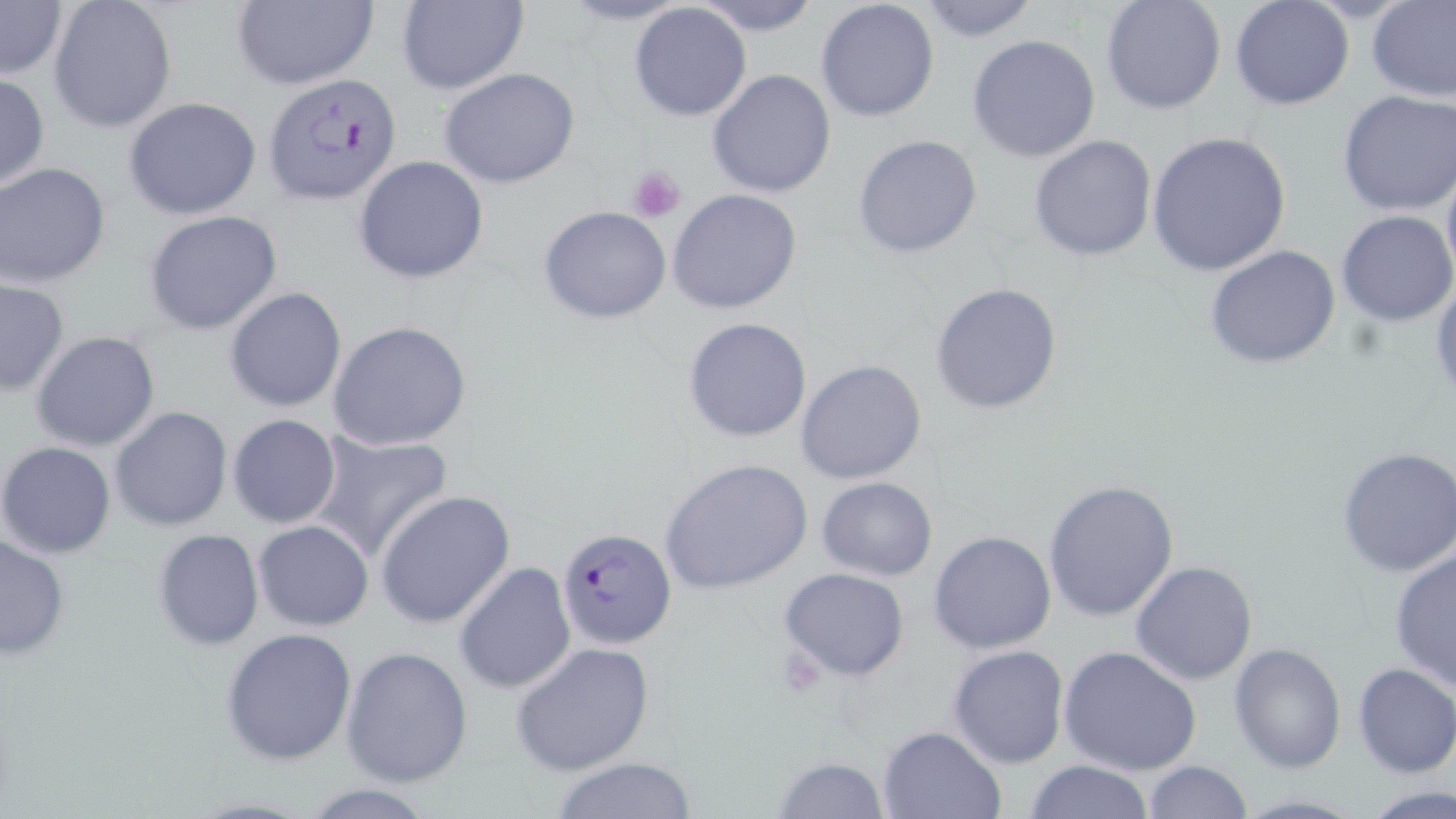

slide_level_diagnosis: Plasmodium falciparum
field_of_view: single
magnification: 1000x
preparation: thin blood smear
stain: May-Grünwald-Giemsa
platelet_locations: 'approximate bounding boxes as named x1/y1/x2/y2 corners in pixels: (x1=627, y1=165, x2=686, y2=221), (x1=774, y1=647, x2=825, y2=693)'
modality: light microscopy
plasmodium_falciparum_infected_red_blood_cell_locations: 'approximate bounding boxes as named x1/y1/x2/y2 corners in pixels: (x1=263, y1=73, x2=405, y2=205), (x1=555, y1=526, x2=676, y2=649)'
uninfected_red_blood_cell_locations: 'approximate bounding boxes as named x1/y1/x2/y2 corners in pixels: (x1=48, y1=0, x2=177, y2=134), (x1=691, y1=0, x2=824, y2=34), (x1=815, y1=0, x2=941, y2=122), (x1=913, y1=0, x2=1041, y2=42), (x1=1099, y1=0, x2=1226, y2=116), (x1=1230, y1=0, x2=1355, y2=111), (x1=229, y1=1, x2=379, y2=90), (x1=393, y1=1, x2=530, y2=94), (x1=1367, y1=1, x2=1456, y2=103), (x1=0, y1=2, x2=67, y2=81), (x1=628, y1=3, x2=752, y2=122), (x1=967, y1=35, x2=1100, y2=162), (x1=439, y1=67, x2=580, y2=188), (x1=707, y1=69, x2=837, y2=196), (x1=0, y1=73, x2=49, y2=191), (x1=1336, y1=91, x2=1456, y2=215), (x1=122, y1=96, x2=261, y2=220), (x1=1146, y1=131, x2=1291, y2=275), (x1=853, y1=133, x2=983, y2=259), (x1=1029, y1=134, x2=1157, y2=261), (x1=354, y1=155, x2=490, y2=284), (x1=1441, y1=163, x2=1456, y2=290), (x1=1, y1=164, x2=111, y2=287), (x1=668, y1=189, x2=803, y2=314), (x1=538, y1=205, x2=672, y2=324), (x1=144, y1=209, x2=284, y2=336), (x1=1336, y1=210, x2=1456, y2=326), (x1=1204, y1=245, x2=1344, y2=371), (x1=0, y1=279, x2=69, y2=395), (x1=931, y1=281, x2=1063, y2=415), (x1=225, y1=287, x2=347, y2=412), (x1=683, y1=316, x2=813, y2=443), (x1=328, y1=319, x2=475, y2=452), (x1=32, y1=331, x2=161, y2=451), (x1=796, y1=359, x2=928, y2=486), (x1=111, y1=407, x2=233, y2=531), (x1=228, y1=414, x2=341, y2=528), (x1=309, y1=430, x2=453, y2=564), (x1=0, y1=441, x2=117, y2=559), (x1=1336, y1=446, x2=1456, y2=578), (x1=660, y1=457, x2=813, y2=596), (x1=816, y1=477, x2=938, y2=581), (x1=1044, y1=479, x2=1180, y2=621), (x1=375, y1=491, x2=516, y2=629), (x1=254, y1=521, x2=373, y2=631), (x1=151, y1=527, x2=264, y2=651), (x1=928, y1=531, x2=1057, y2=654), (x1=0, y1=535, x2=70, y2=662), (x1=1389, y1=547, x2=1456, y2=693), (x1=1130, y1=560, x2=1257, y2=685), (x1=454, y1=563, x2=577, y2=694), (x1=779, y1=567, x2=910, y2=681), (x1=220, y1=627, x2=358, y2=765), (x1=1228, y1=641, x2=1345, y2=773), (x1=510, y1=642, x2=656, y2=776), (x1=947, y1=644, x2=1070, y2=767), (x1=1059, y1=645, x2=1204, y2=775), (x1=341, y1=646, x2=473, y2=785), (x1=1352, y1=662, x2=1456, y2=778), (x1=877, y1=725, x2=1006, y2=818), (x1=549, y1=757, x2=703, y2=817), (x1=772, y1=757, x2=892, y2=817), (x1=1024, y1=760, x2=1156, y2=819), (x1=1144, y1=760, x2=1252, y2=818), (x1=296, y1=783, x2=440, y2=819), (x1=1362, y1=784, x2=1456, y2=818)'
image_size: 1456×819 pixels